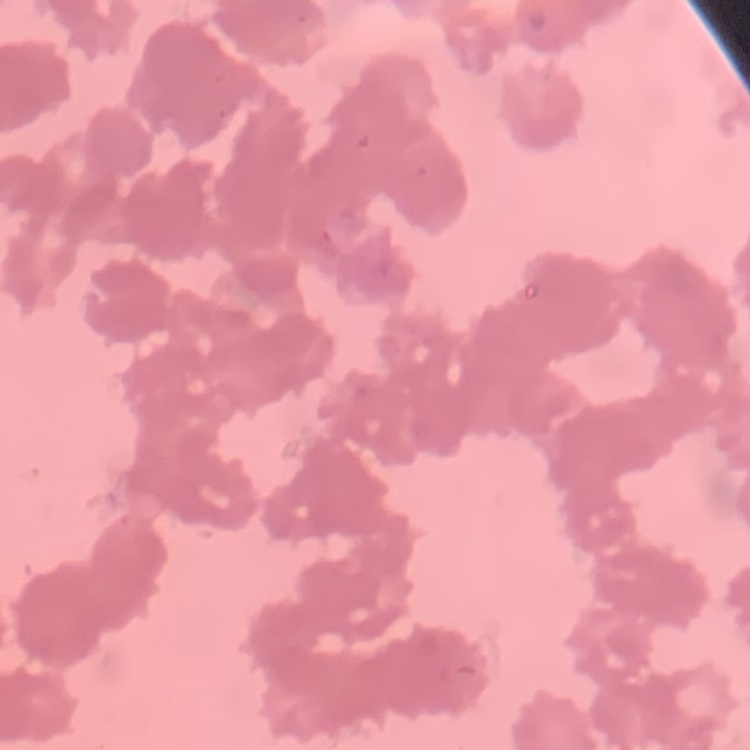
red blood cell morphology = rouleaux formation
preparation = thin blood film
stain = Field's or Giemsa
image type = one tile cut from a larger photomicrograph